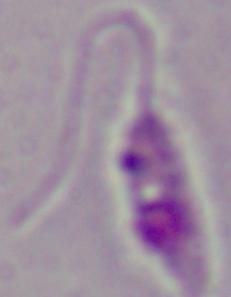
Summary:
  - Modality: photomicrograph
  - Identification: Leishmania
  - Magnification: 1000x